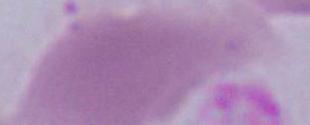
Captured at 1000x magnification. Micrograph. A red blood cell is shown.